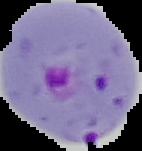

Summary:
  - Result: malaria parasites detected
  - Image size: 142×151 pixels
  - Image type: cell region segmented out of the field of view; surrounding area masked to black
  - Preparation: thin blood smear